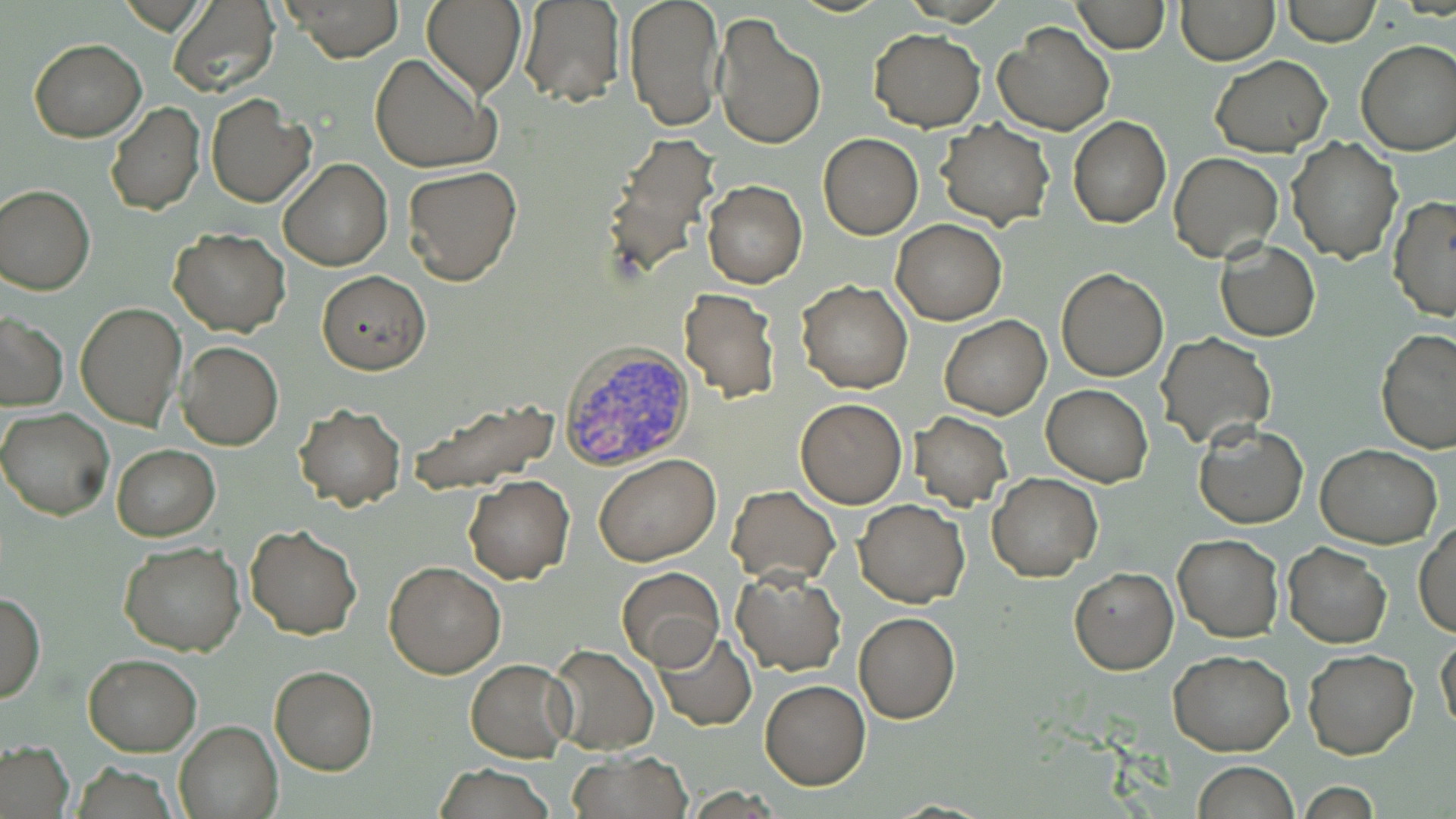 Approximate bounding boxes as [x1, y1, x2, y2] in pixels. Uninfected red blood cell locations: [285, 0, 401, 61], [421, 0, 527, 96], [622, 0, 725, 131], [1071, 0, 1170, 53], [1175, 0, 1279, 65], [1280, 0, 1379, 45], [167, 1, 280, 97], [519, 1, 624, 106], [713, 13, 828, 152], [992, 21, 1114, 135], [868, 29, 986, 132], [29, 38, 146, 142], [1355, 38, 1456, 157], [370, 51, 500, 175], [1209, 55, 1331, 156], [205, 94, 315, 208], [105, 103, 205, 216], [1068, 115, 1171, 229], [935, 121, 1055, 229], [601, 132, 724, 276], [818, 134, 924, 239], [1287, 138, 1400, 262], [1168, 150, 1282, 263], [279, 160, 392, 271], [403, 165, 523, 285], [702, 179, 807, 288], [0, 183, 96, 295], [1387, 197, 1456, 322], [891, 219, 1007, 325], [168, 227, 290, 336], [1215, 241, 1320, 342], [1057, 268, 1169, 381], [317, 271, 431, 374], [796, 279, 913, 393], [679, 287, 781, 403], [76, 301, 187, 432], [1, 313, 68, 410], [940, 314, 1052, 419], [1376, 328, 1456, 455], [1157, 333, 1275, 448], [177, 342, 283, 449], [1042, 385, 1152, 486], [407, 398, 561, 496], [795, 398, 906, 508], [294, 403, 405, 510], [0, 408, 114, 521], [909, 412, 1013, 511], [1194, 421, 1308, 529], [112, 444, 220, 541], [1315, 444, 1442, 548], [594, 455, 720, 567], [987, 472, 1103, 581], [463, 474, 574, 584], [727, 485, 840, 586], [853, 499, 969, 607], [1414, 520, 1456, 637], [246, 524, 361, 640], [1172, 533, 1283, 642], [118, 542, 246, 656], [1283, 543, 1392, 649], [384, 561, 505, 678], [615, 566, 726, 670], [1068, 566, 1178, 675], [732, 568, 846, 676], [0, 591, 45, 704], [853, 612, 961, 724], [652, 629, 756, 729], [1435, 636, 1456, 734], [547, 644, 659, 755], [1303, 648, 1418, 759], [1168, 651, 1294, 755], [82, 652, 202, 755], [465, 659, 575, 762], [269, 666, 377, 775], [759, 679, 870, 790], [174, 720, 284, 819], [0, 741, 75, 818], [569, 750, 693, 819], [1191, 761, 1299, 818], [430, 764, 558, 819]. Plasmodium vivax-infected red blood cell locations: [557, 343, 695, 473]. Slide-level diagnosis: Plasmodium vivax. Image is 1456×819 pixels. Captured at 1000x magnification. May-Grünwald-Giemsa stain. Thin blood smear. Optical microscopy. Single field of view.